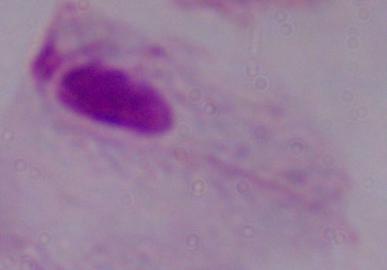

magnification = 1000x
identification = trichomonad
modality = micrograph